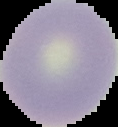

image size = 118×127 pixels
result = no Plasmodium parasites detected
preparation = thin blood film
image type = segmented cell region with the area outside set to black